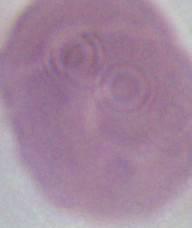 Captured at 1000x magnification. An erythrocyte is seen. Micrograph.